Report the malaria status of this cell.
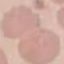

Uninfected.

Summary:
  - Preparation: thin blood smear
  - Image type: automatically extracted cell patch, resized to 64 × 64 pixels
  - Capture: smartphone camera at the microscope eyepiece
  - Stain: Giemsa